Assess this cell for malaria.
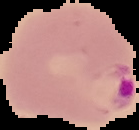
Parasitized.

image type = segmented cell region with the area outside set to black
preparation = thin blood film
image size = 139×130 pixels